Locate and identify every blood parasite.
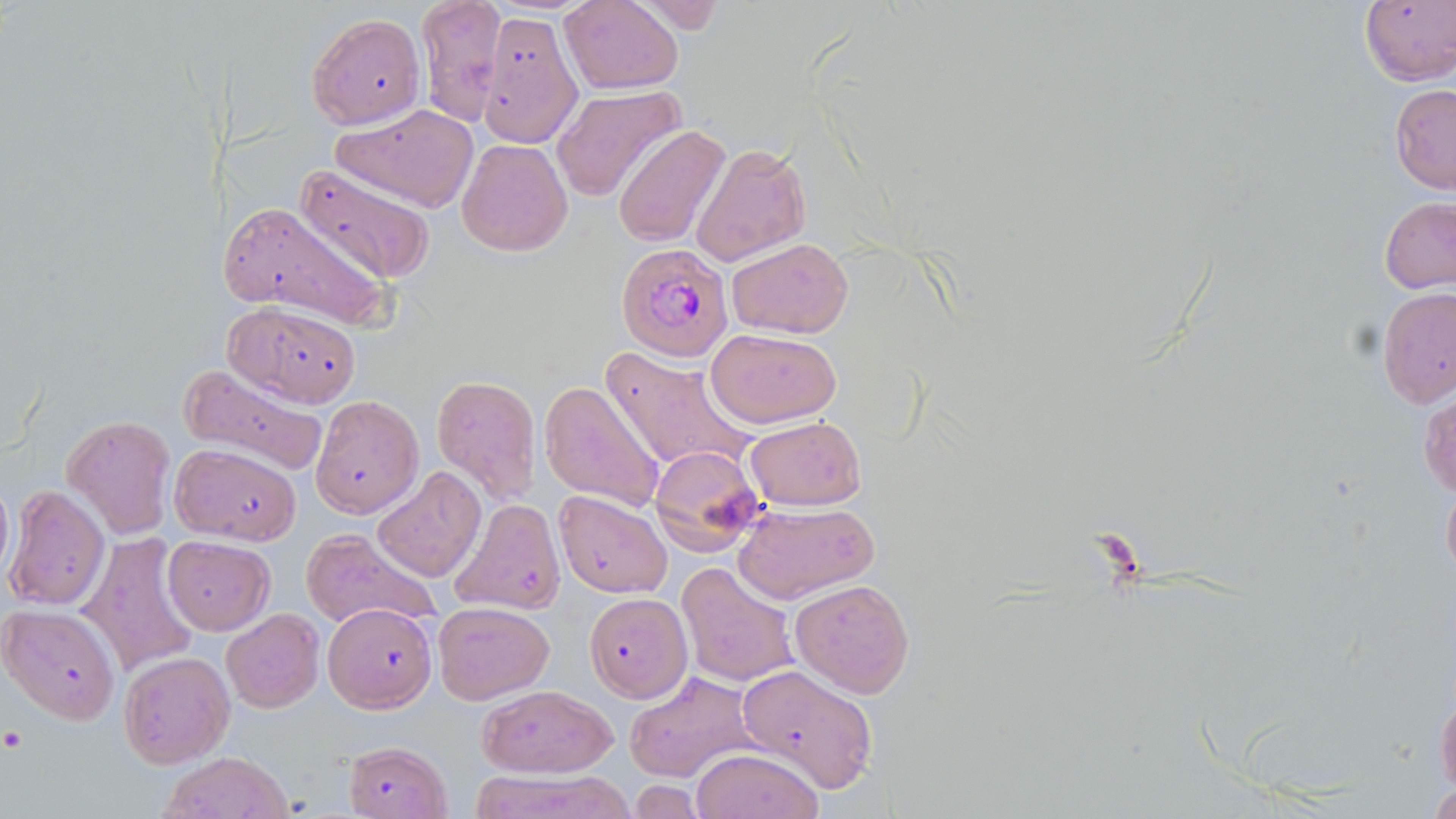

Approximate bounding boxes as (x1, y1, x2, y2) in pixels.
Plasmodium falciparum-infected red blood cells (subset): (615, 242, 731, 362).
No Plasmodium ovale, Plasmodium malariae, Plasmodium vivax, Babesia divergens, or Trypanosoma brucei observed.

Platelet locations: (2, 727, 26, 753). Uninfected red blood cell locations (subset): (417, 0, 505, 128), (561, 0, 684, 94), (1358, 0, 1456, 87), (308, 12, 424, 129), (1389, 84, 1456, 195), (552, 86, 683, 205), (333, 104, 480, 211), (613, 127, 729, 248), (456, 138, 573, 257), (691, 143, 811, 267), (292, 163, 439, 285), (1379, 196, 1456, 295), (219, 198, 390, 331), (726, 237, 854, 340), (1377, 286, 1456, 408), (225, 302, 362, 406), (706, 329, 844, 427), (603, 347, 756, 478), (177, 362, 330, 477), (430, 375, 542, 501), (540, 380, 666, 512), (1419, 391, 1455, 499), (311, 394, 425, 519), (62, 416, 175, 538), (745, 416, 868, 510), (170, 444, 302, 544), (648, 445, 767, 555), (373, 467, 486, 582), (0, 475, 13, 587), (1441, 475, 1456, 589), (6, 484, 110, 612), (554, 492, 672, 597), (449, 499, 565, 618), (734, 501, 879, 604), (299, 528, 439, 631), (78, 532, 201, 677), (162, 535, 275, 635), (675, 561, 799, 688), (790, 577, 914, 699), (585, 595, 685, 704), (433, 600, 556, 705), (322, 602, 438, 711), (1, 605, 121, 724), (221, 609, 324, 712), (117, 650, 236, 769), (737, 663, 879, 793), (624, 671, 757, 783), (1433, 671, 1456, 798), (476, 684, 616, 778), (340, 739, 455, 819), (689, 748, 823, 819), (157, 751, 296, 819), (465, 768, 637, 819), (627, 779, 707, 816), (1424, 781, 1456, 818). Slide-level diagnosis: Plasmodium falciparum. May-Grünwald-Giemsa stain. Thin blood smear. Optical microscopy. 1000x magnification. Single field of view. Image is 1456×819 pixels.